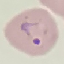
result: malaria parasites detected
preparation: thin smear
stain: Giemsa
capture: smartphone through the microscope eyepiece
image_type: automatically extracted cell patch, resized to 64 × 64 pixels